Identify the parasite.
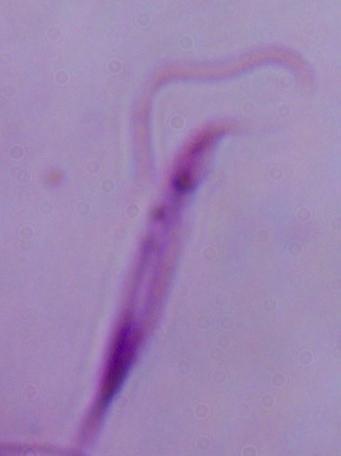
Leishmania.

Summary:
  - Modality: micrograph
  - Magnification: 1000x